Classify this cell by malaria status.
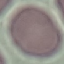

It is uninfected.

image type = automatically extracted cell patch, resized to 64 × 64 pixels
stain = Giemsa
preparation = thin smear
capture = smartphone through the microscope eyepiece